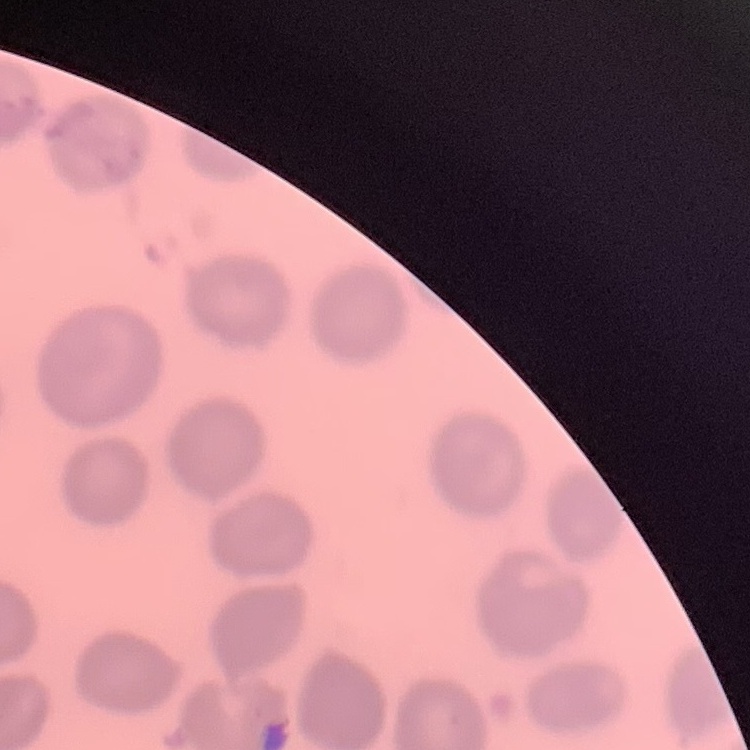
red_blood_cell_morphology: no rouleaux formation
image_type: one tile cut from a larger photomicrograph
preparation: thin blood smear
stain: Field's or Giemsa